Name the blood parasite species.
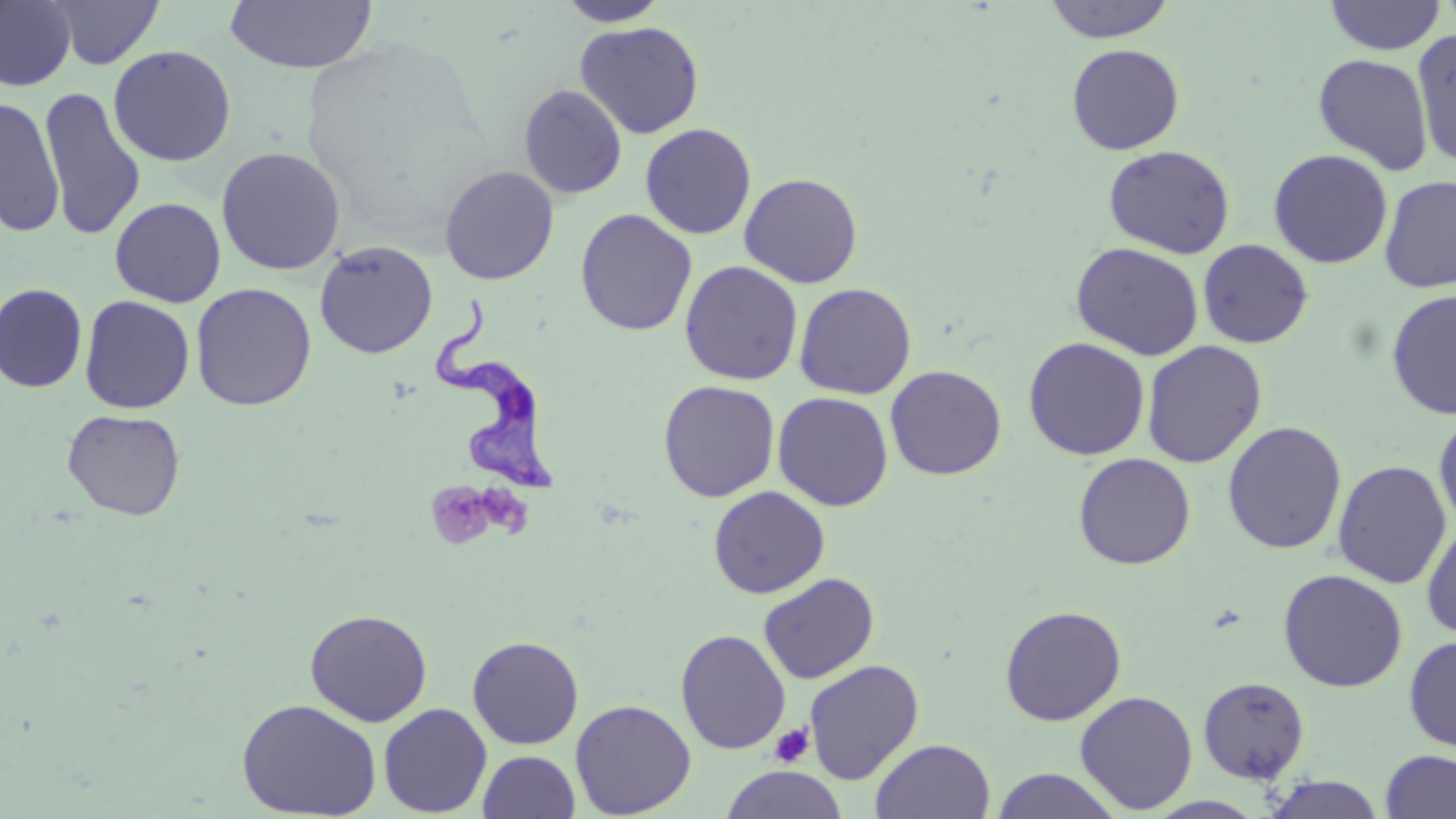

Trypanosoma brucei.

uninfected red blood cell locations = approximate bounding boxes as named x1/y1/x2/y2 corners in pixels: (x1=0, y1=0, x2=77, y2=90), (x1=45, y1=0, x2=165, y2=69), (x1=225, y1=0, x2=377, y2=75), (x1=556, y1=0, x2=670, y2=26), (x1=1043, y1=0, x2=1176, y2=43), (x1=1325, y1=0, x2=1447, y2=55), (x1=576, y1=21, x2=704, y2=139), (x1=1411, y1=27, x2=1456, y2=169), (x1=1067, y1=43, x2=1185, y2=154), (x1=108, y1=44, x2=236, y2=167), (x1=1312, y1=53, x2=1433, y2=175), (x1=518, y1=83, x2=627, y2=199), (x1=39, y1=86, x2=146, y2=241), (x1=0, y1=96, x2=65, y2=237), (x1=640, y1=123, x2=756, y2=239), (x1=1104, y1=144, x2=1236, y2=259), (x1=216, y1=146, x2=346, y2=275), (x1=1268, y1=149, x2=1392, y2=268), (x1=440, y1=166, x2=559, y2=285), (x1=739, y1=172, x2=863, y2=288), (x1=1379, y1=175, x2=1456, y2=293), (x1=109, y1=197, x2=226, y2=307), (x1=575, y1=209, x2=697, y2=337), (x1=1198, y1=239, x2=1313, y2=349), (x1=314, y1=240, x2=438, y2=359), (x1=1071, y1=242, x2=1204, y2=360), (x1=680, y1=260, x2=803, y2=386), (x1=0, y1=283, x2=88, y2=392), (x1=191, y1=283, x2=316, y2=411), (x1=794, y1=283, x2=917, y2=399), (x1=1386, y1=289, x2=1456, y2=419), (x1=79, y1=295, x2=195, y2=414), (x1=1023, y1=337, x2=1150, y2=461), (x1=1141, y1=340, x2=1267, y2=468), (x1=885, y1=364, x2=1007, y2=481), (x1=658, y1=380, x2=780, y2=502), (x1=773, y1=391, x2=894, y2=511), (x1=62, y1=409, x2=186, y2=521), (x1=1434, y1=410, x2=1456, y2=531), (x1=1223, y1=421, x2=1347, y2=554), (x1=1073, y1=453, x2=1196, y2=570), (x1=1333, y1=460, x2=1451, y2=588), (x1=708, y1=486, x2=830, y2=599), (x1=1421, y1=518, x2=1456, y2=641), (x1=1277, y1=568, x2=1408, y2=692), (x1=758, y1=572, x2=879, y2=684), (x1=999, y1=605, x2=1127, y2=726), (x1=304, y1=608, x2=433, y2=726), (x1=675, y1=629, x2=791, y2=755), (x1=467, y1=635, x2=584, y2=749), (x1=1403, y1=635, x2=1456, y2=752), (x1=803, y1=659, x2=925, y2=785), (x1=1198, y1=676, x2=1309, y2=784), (x1=1075, y1=690, x2=1198, y2=814), (x1=236, y1=698, x2=382, y2=819), (x1=570, y1=698, x2=696, y2=817), (x1=378, y1=703, x2=492, y2=817), (x1=871, y1=739, x2=995, y2=819), (x1=478, y1=750, x2=580, y2=819), (x1=1381, y1=750, x2=1456, y2=818), (x1=721, y1=765, x2=848, y2=819), (x1=991, y1=768, x2=1122, y2=818), (x1=1263, y1=775, x2=1387, y2=818)
magnification = 1000x
image size = 1456×819 pixels
Trypanosoma brucei locations = approximate bounding boxes as named x1/y1/x2/y2 corners in pixels: (x1=433, y1=290, x2=563, y2=497)
stain = May-Grünwald-Giemsa
field of view = single
preparation = thin blood film
modality = light microscopy
platelet locations = approximate bounding boxes as named x1/y1/x2/y2 corners in pixels: (x1=425, y1=480, x2=497, y2=548), (x1=770, y1=724, x2=814, y2=767)